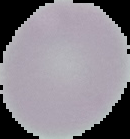
preparation = thin blood smear
image type = segmented cell region on a black background
image size = 130×139 pixels
malaria status = uninfected